Point out each Plasmodium parasite.
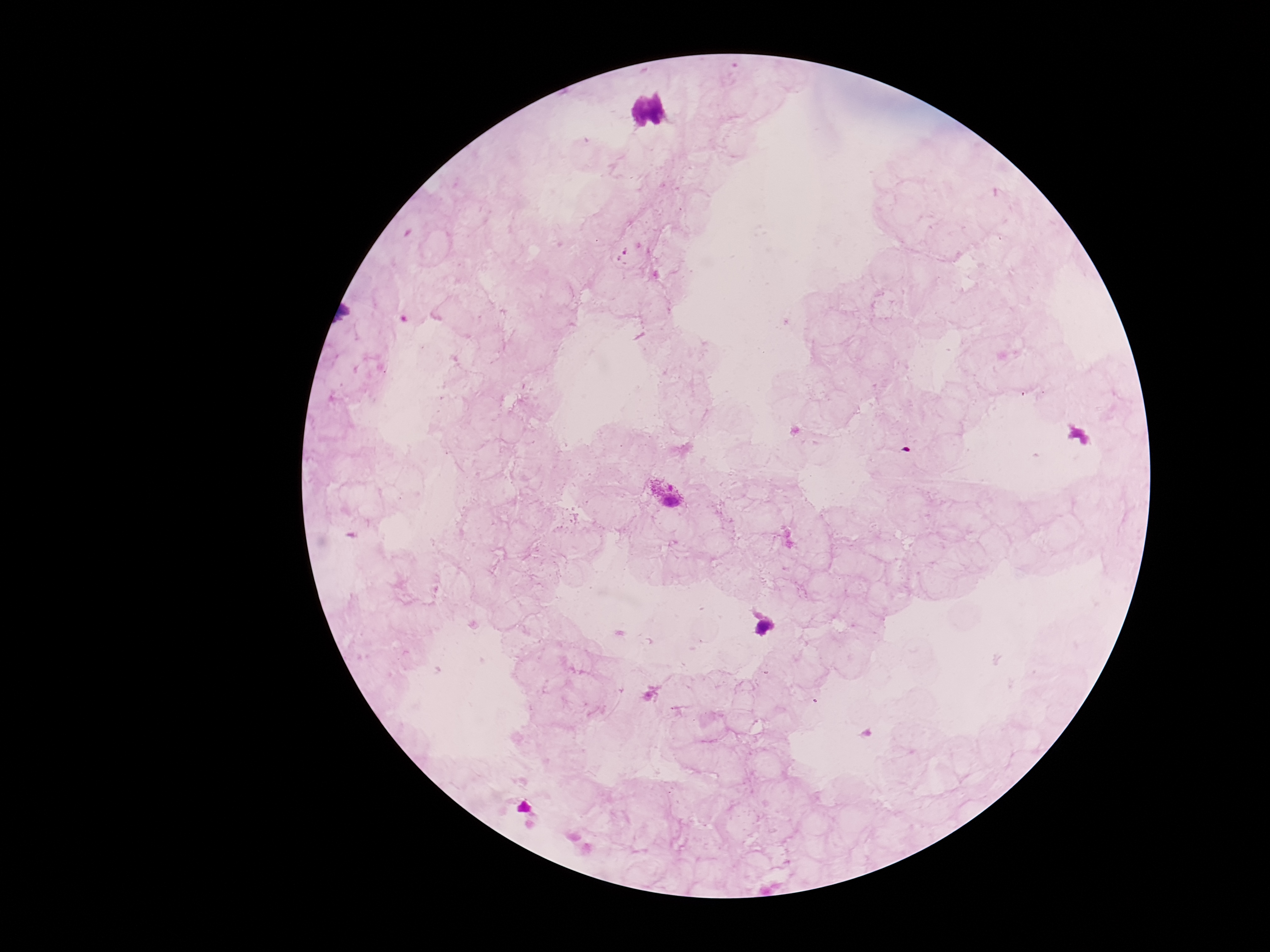

Approximate centers as {x, y} in pixels.
Plasmodium parasites: {668, 494}.

Smartphone photograph taken through the microscope eyepiece. 100x magnification. Image is 1270×952 pixels. One field from this slide. Giemsa stain. Thick peripheral-blood smear. Patient malaria status: infected.